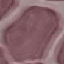
Summary:
  - Malaria status: uninfected
  - Stain: Giemsa
  - Image type: automatically extracted cell patch, resized to 64 × 64 pixels
  - Preparation: thin blood smear
  - Capture: smartphone camera at the microscope eyepiece